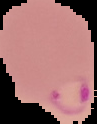

From a thin blood smear. Image is 97×124 pixels. Malaria status: parasitized. Cell region segmented out of the field of view; the surrounding area is masked to black.